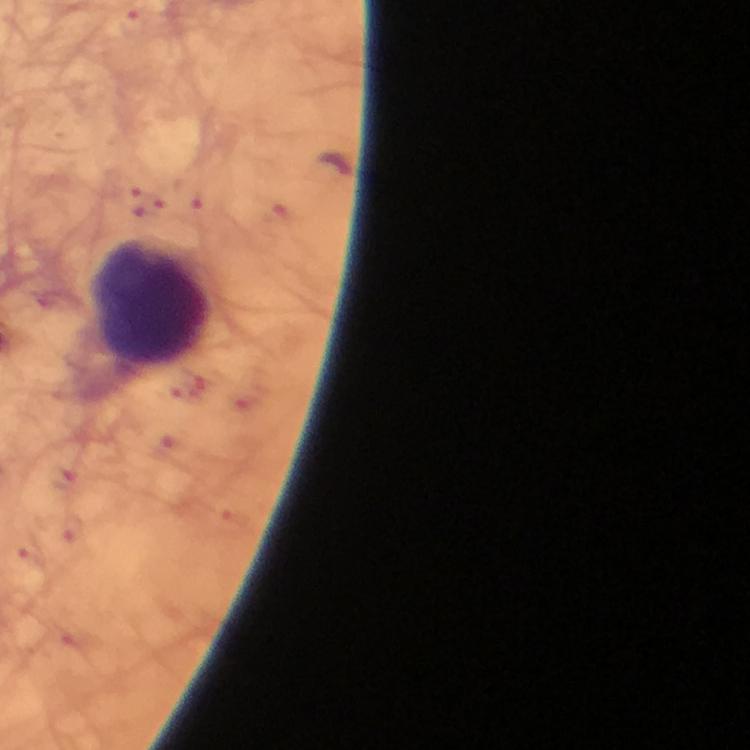

Plasmodium parasite locations = approximate object centers, in pixels from the top-left corner: (x=334, y=163)
cropped from = one field of view
magnification = 100x
image size = 750×750 pixels
preparation = thick blood film
context = from a diagnostic examination for malaria
capture = smartphone camera through the microscope
leukocyte locations = approximate object centers, in pixels from the top-left corner: (x=150, y=303)
immersion oil = applied
stain = Giemsa